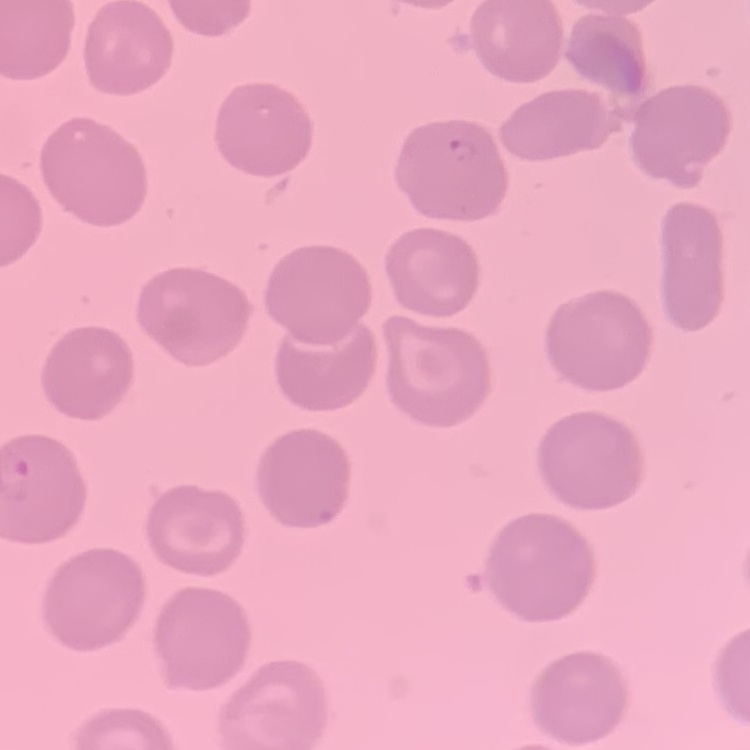

red_blood_cell_morphology: no rouleaux formation
preparation: thin blood smear
image_type: one tile cut from a larger photomicrograph
stain: Field's or Giemsa